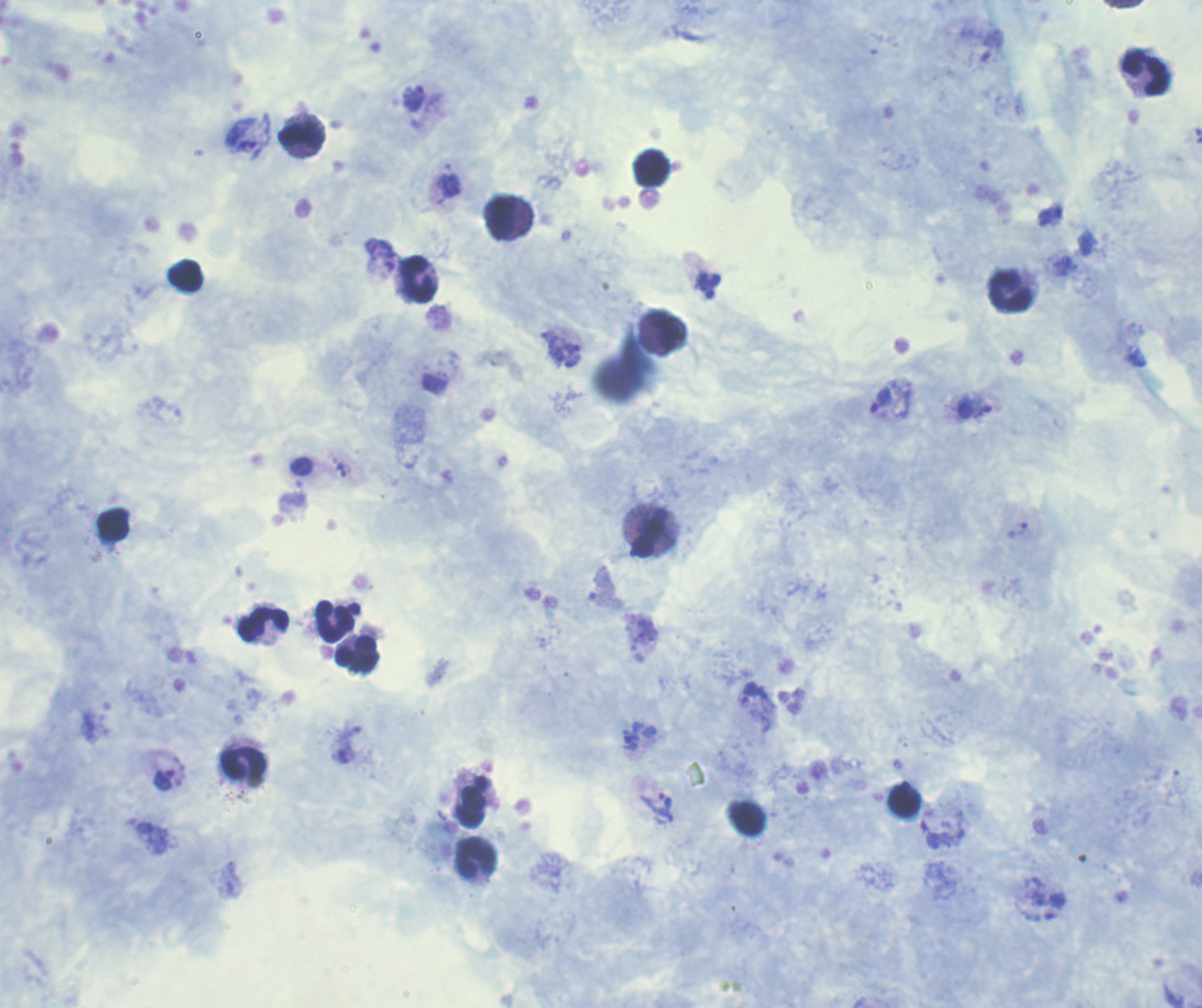
preparation: thick blood film
leukocyte_locations: 'approximate centers as {x, y} in pixels: {1147, 72}, {301, 137}, {652, 168}, {501, 218}, {186, 275}, {417, 279}, {1010, 291}, {667, 328}, {115, 524}, {649, 534}, {335, 621}, {264, 624}, {357, 654}, {243, 762}, {905, 801}, {472, 806}, {476, 857}'
result: Plasmodium parasites identified
stain: Romanowsky
trophozoite_locations: 'approximate centers as {x, y} in pixels: {413, 97}, {247, 145}, {380, 254}, {572, 354}, {881, 400}, {1018, 530}, {754, 692}, {631, 740}, {165, 780}, {666, 800}, {663, 816}'
magnification: 100x
context: previously used in an actual diagnosis
coloration_quality: good
field_of_view: single
background_quality: satisfactory
image_size: 1202×1008 pixels